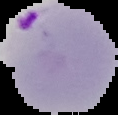
From a thin blood film. The area outside the segmented cell region is set to black. Image is 118×115 pixels. Result: malaria parasites detected.